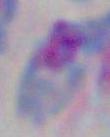 Captured at 1000x magnification. Toxoplasma gondii is seen. Photomicrograph.